Classify this cell by malaria status.
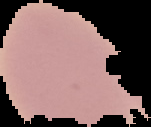
Uninfected.

preparation = thin blood film
image size = 151×127 pixels
image type = segmented cell region with the area outside set to black